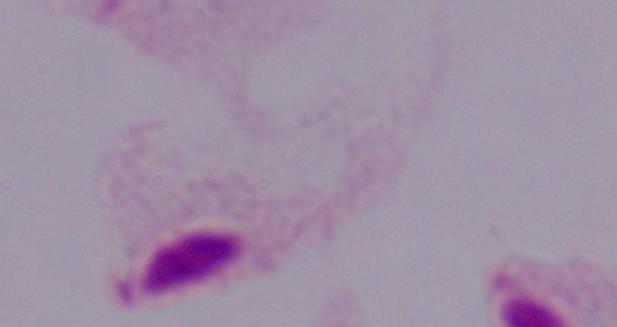

Summary:
  - Magnification: 1000x
  - Identification: trichomonad
  - Modality: micrograph